Assess the morphology of the red blood cells.
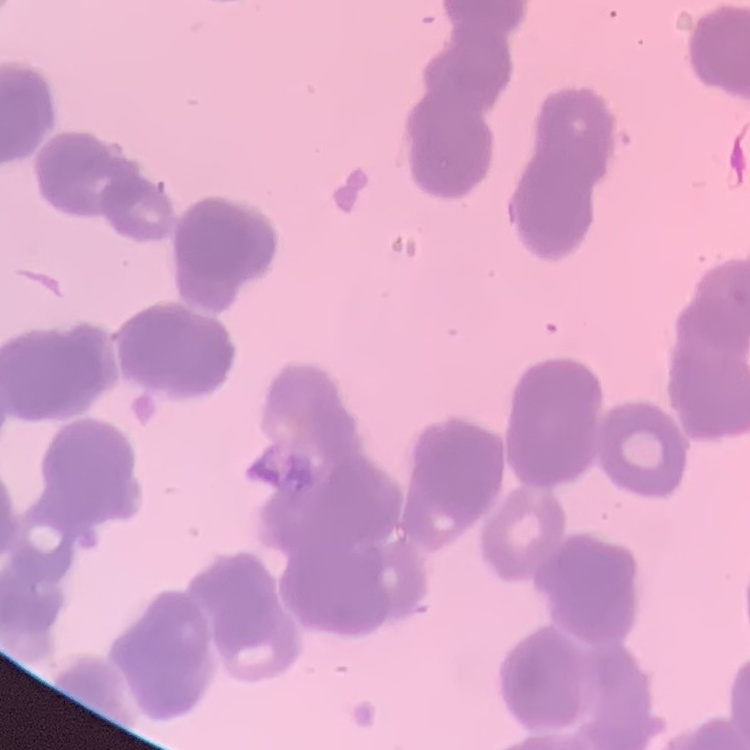
They show rouleaux formation.

Square crop of a larger photomicrograph. Stained with either Field's or Giemsa. Thin peripheral smear.